Name the cell type shown.
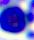
This is a leukocyte.

Captured at 400x magnification. Micrograph.